Describe the morphology of the red blood cells.
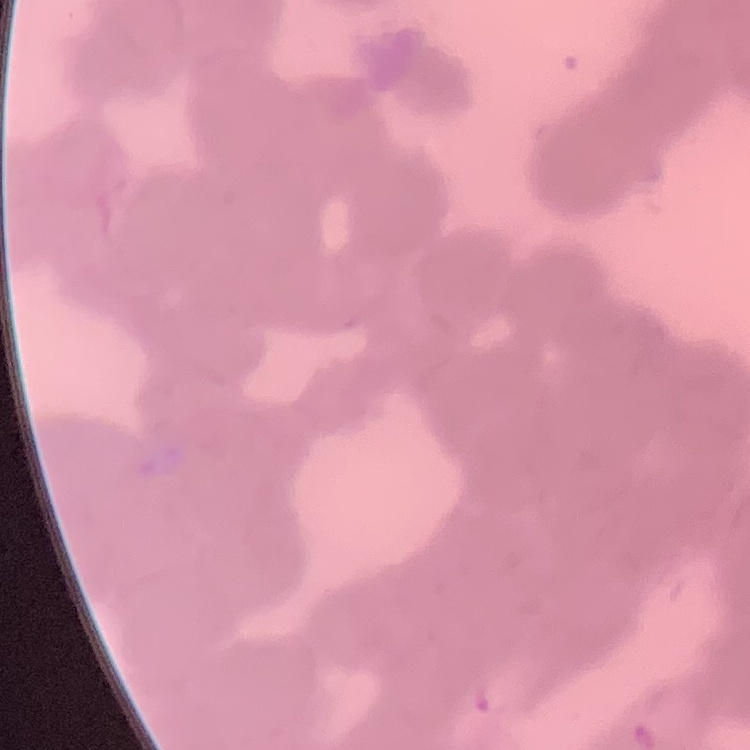
Rouleaux formation.

Thin blood film. Square crop of a larger photomicrograph. Stained with either Field's or Giemsa.